Name the parasite shown.
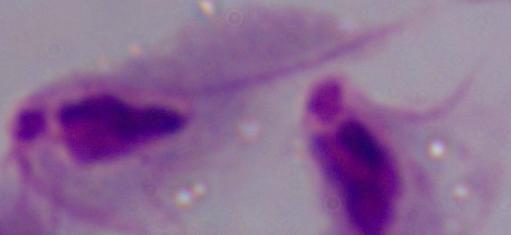
A trichomonad.

1000x magnification. Micrograph.